Comment on the morphology of the erythrocytes.
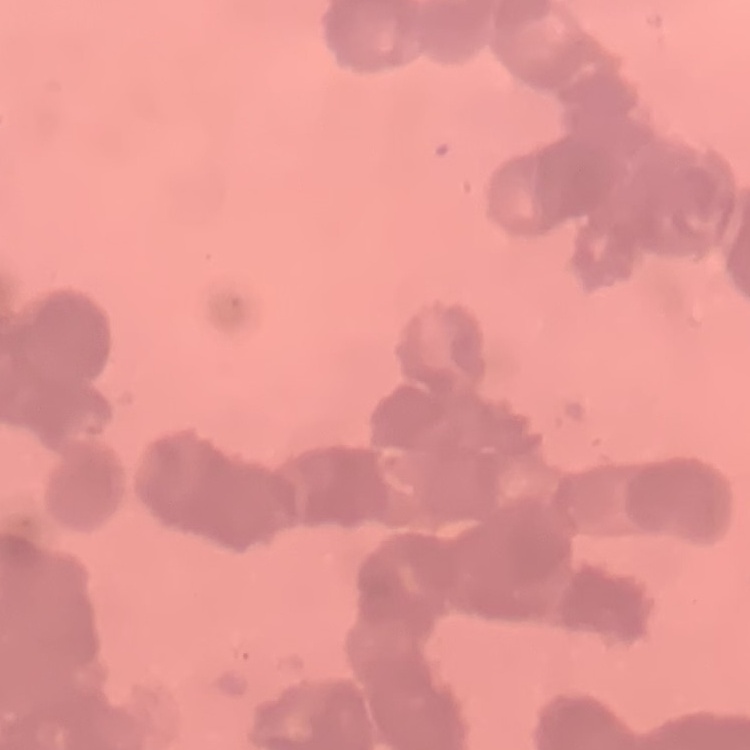
Rouleaux formation.

stain: Field's or Giemsa
preparation: thin blood smear
image_type: one tile cut from a larger photomicrograph